Point out each Plasmodium parasite.
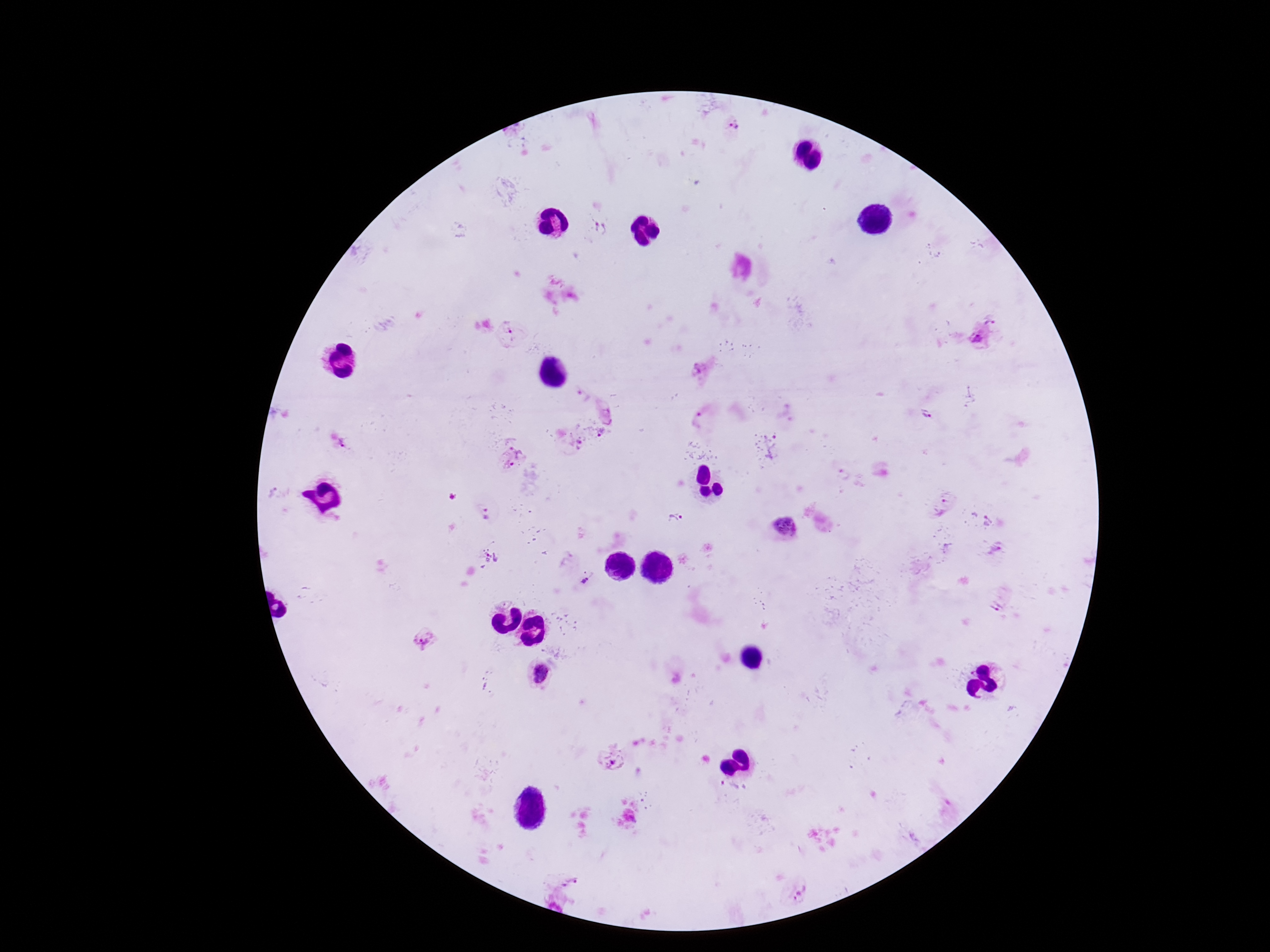
Approximate centers as (x, y) in pixels.
Plasmodium parasites: (734, 127), (602, 227), (992, 323), (511, 332), (977, 336), (702, 370), (580, 395), (605, 411), (927, 414), (703, 416), (602, 430), (342, 443), (579, 444), (772, 446), (518, 447), (506, 466), (840, 473), (271, 492), (947, 507), (487, 512), (675, 519), (988, 519), (784, 527), (996, 550), (493, 558), (587, 578), (996, 600), (426, 640), (543, 674), (609, 757), (728, 790), (570, 882), (800, 893).

Summary:
  - Preparation: thick blood film
  - Image size: 1270×952 pixels
  - Stain: Giemsa
  - Field of view: single
  - Patient malaria status: infected
  - Capture: smartphone camera through the microscope eyepiece
  - Magnification: 100x